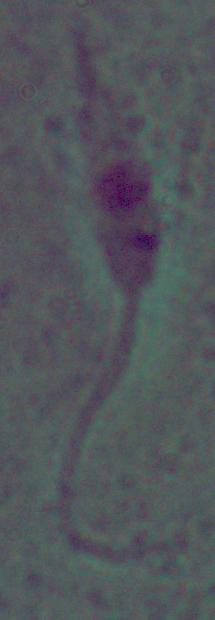
Summary:
  - Identification: Leishmania
  - Modality: photomicrograph
  - Magnification: 1000x